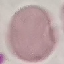
Malaria status: uninfected. Giemsa stain. Photographed with a smartphone camera at the microscope eyepiece. Thin blood smear. Cell patch, automatically extracted from a larger field of view and resized to 64 × 64 pixels.